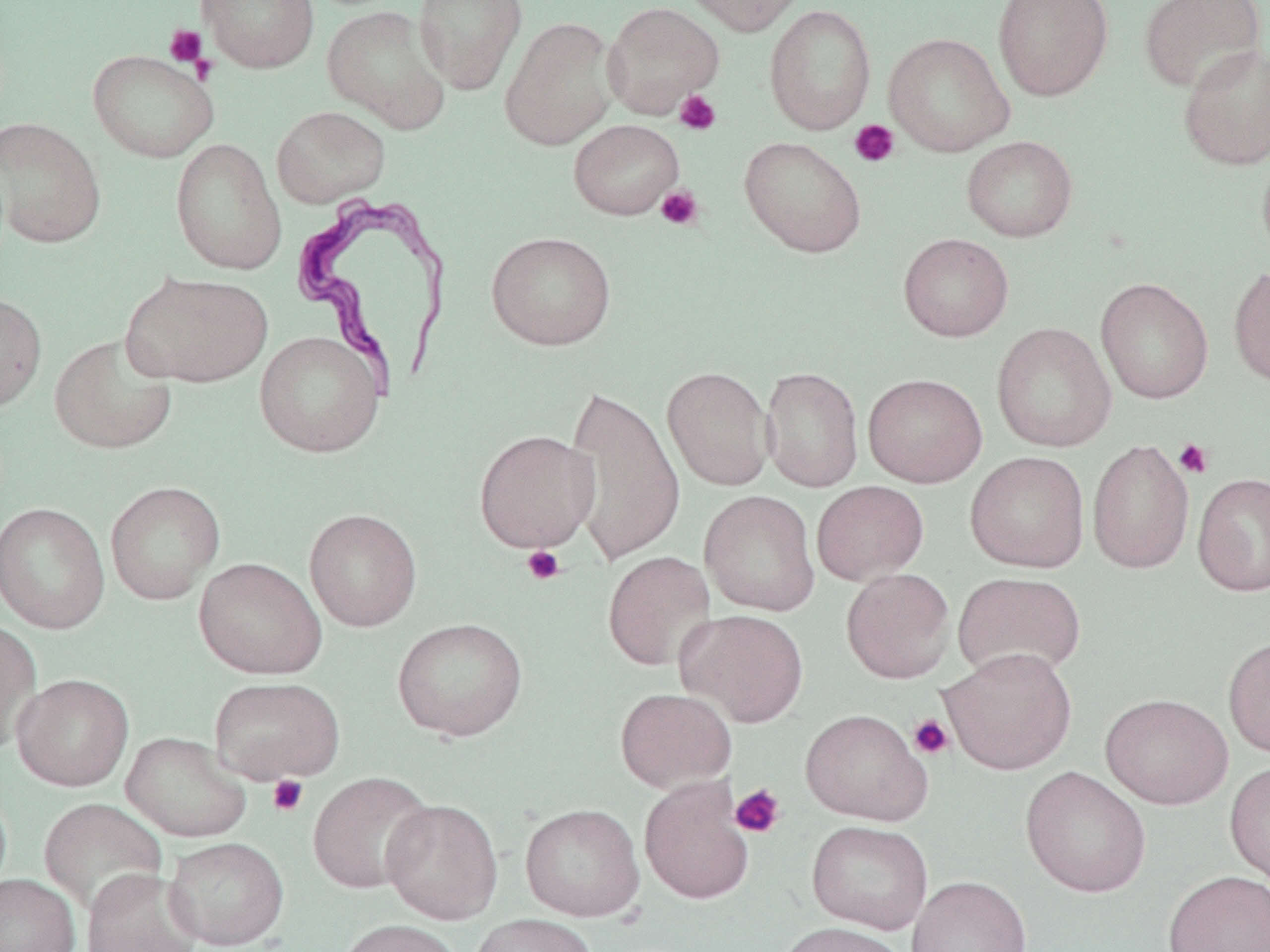

Approximate bounding boxes as named x1/y1/x2/y2 corners in pixels. Platelet locations: (x1=164, y1=24, x2=206, y2=67), (x1=674, y1=90, x2=721, y2=135), (x1=849, y1=120, x2=900, y2=168), (x1=656, y1=186, x2=704, y2=230), (x1=1174, y1=438, x2=1214, y2=479), (x1=521, y1=545, x2=565, y2=586), (x1=908, y1=714, x2=954, y2=760), (x1=267, y1=775, x2=309, y2=817), (x1=729, y1=784, x2=786, y2=838). Uninfected red blood cell locations: (x1=196, y1=0, x2=319, y2=73), (x1=413, y1=0, x2=527, y2=95), (x1=679, y1=0, x2=807, y2=36), (x1=992, y1=0, x2=1113, y2=101), (x1=1139, y1=0, x2=1266, y2=94), (x1=601, y1=2, x2=725, y2=118), (x1=321, y1=4, x2=452, y2=133), (x1=764, y1=4, x2=877, y2=135), (x1=500, y1=17, x2=620, y2=150), (x1=884, y1=33, x2=1015, y2=157), (x1=1177, y1=43, x2=1270, y2=171), (x1=88, y1=49, x2=219, y2=163), (x1=271, y1=105, x2=390, y2=208), (x1=0, y1=117, x2=107, y2=248), (x1=568, y1=119, x2=684, y2=220), (x1=961, y1=135, x2=1078, y2=242), (x1=739, y1=136, x2=867, y2=257), (x1=170, y1=138, x2=287, y2=275), (x1=1256, y1=149, x2=1270, y2=265), (x1=486, y1=231, x2=617, y2=350), (x1=898, y1=233, x2=1014, y2=341), (x1=1228, y1=264, x2=1270, y2=387), (x1=122, y1=271, x2=273, y2=388), (x1=1096, y1=278, x2=1214, y2=404), (x1=0, y1=292, x2=47, y2=413), (x1=991, y1=323, x2=1117, y2=452), (x1=254, y1=330, x2=385, y2=459), (x1=49, y1=332, x2=179, y2=455), (x1=662, y1=366, x2=774, y2=491), (x1=760, y1=366, x2=864, y2=493), (x1=862, y1=372, x2=987, y2=488), (x1=562, y1=384, x2=686, y2=566), (x1=474, y1=429, x2=600, y2=552), (x1=1087, y1=438, x2=1194, y2=574), (x1=965, y1=451, x2=1090, y2=572), (x1=1192, y1=472, x2=1270, y2=597), (x1=105, y1=480, x2=226, y2=604), (x1=811, y1=481, x2=929, y2=585), (x1=699, y1=490, x2=820, y2=616), (x1=0, y1=502, x2=110, y2=634), (x1=304, y1=508, x2=422, y2=631), (x1=602, y1=551, x2=716, y2=671), (x1=194, y1=557, x2=326, y2=679), (x1=841, y1=568, x2=955, y2=683), (x1=952, y1=571, x2=1086, y2=683), (x1=676, y1=609, x2=809, y2=728), (x1=0, y1=617, x2=42, y2=755), (x1=392, y1=617, x2=527, y2=742), (x1=1223, y1=635, x2=1270, y2=758), (x1=939, y1=647, x2=1077, y2=774), (x1=12, y1=673, x2=134, y2=791), (x1=209, y1=677, x2=345, y2=785), (x1=615, y1=687, x2=736, y2=792), (x1=1100, y1=693, x2=1233, y2=809), (x1=800, y1=709, x2=933, y2=825), (x1=121, y1=731, x2=251, y2=842), (x1=1224, y1=759, x2=1270, y2=889), (x1=1020, y1=766, x2=1151, y2=898), (x1=307, y1=772, x2=436, y2=894), (x1=639, y1=777, x2=755, y2=904), (x1=38, y1=798, x2=167, y2=916), (x1=381, y1=799, x2=503, y2=923), (x1=520, y1=803, x2=645, y2=922), (x1=807, y1=820, x2=933, y2=934), (x1=164, y1=836, x2=289, y2=950), (x1=81, y1=868, x2=203, y2=952), (x1=1163, y1=869, x2=1270, y2=952), (x1=0, y1=873, x2=81, y2=952), (x1=906, y1=875, x2=1032, y2=952), (x1=469, y1=913, x2=597, y2=952), (x1=335, y1=918, x2=464, y2=952), (x1=774, y1=921, x2=910, y2=952). Trypanosoma brucei locations: (x1=290, y1=194, x2=454, y2=399). Slide-level diagnosis: Trypanosoma brucei. Image is 1270×952 pixels. May-Grünwald-Giemsa stain. Optical microscopy. One field of a larger specimen. Thin blood smear. Captured at 1000x magnification.